Name the parasite shown.
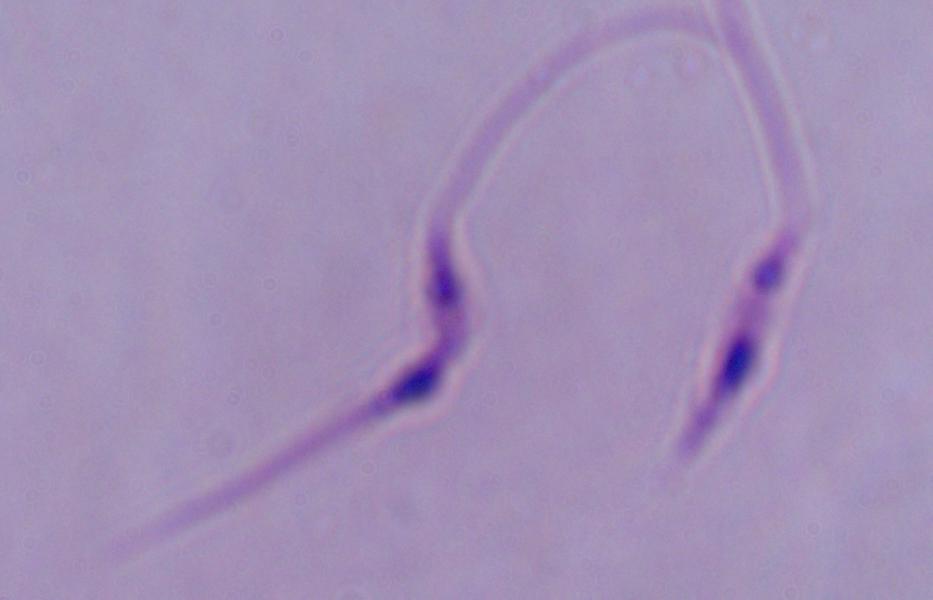
This is Leishmania.

Captured at 1000x magnification. Micrograph.